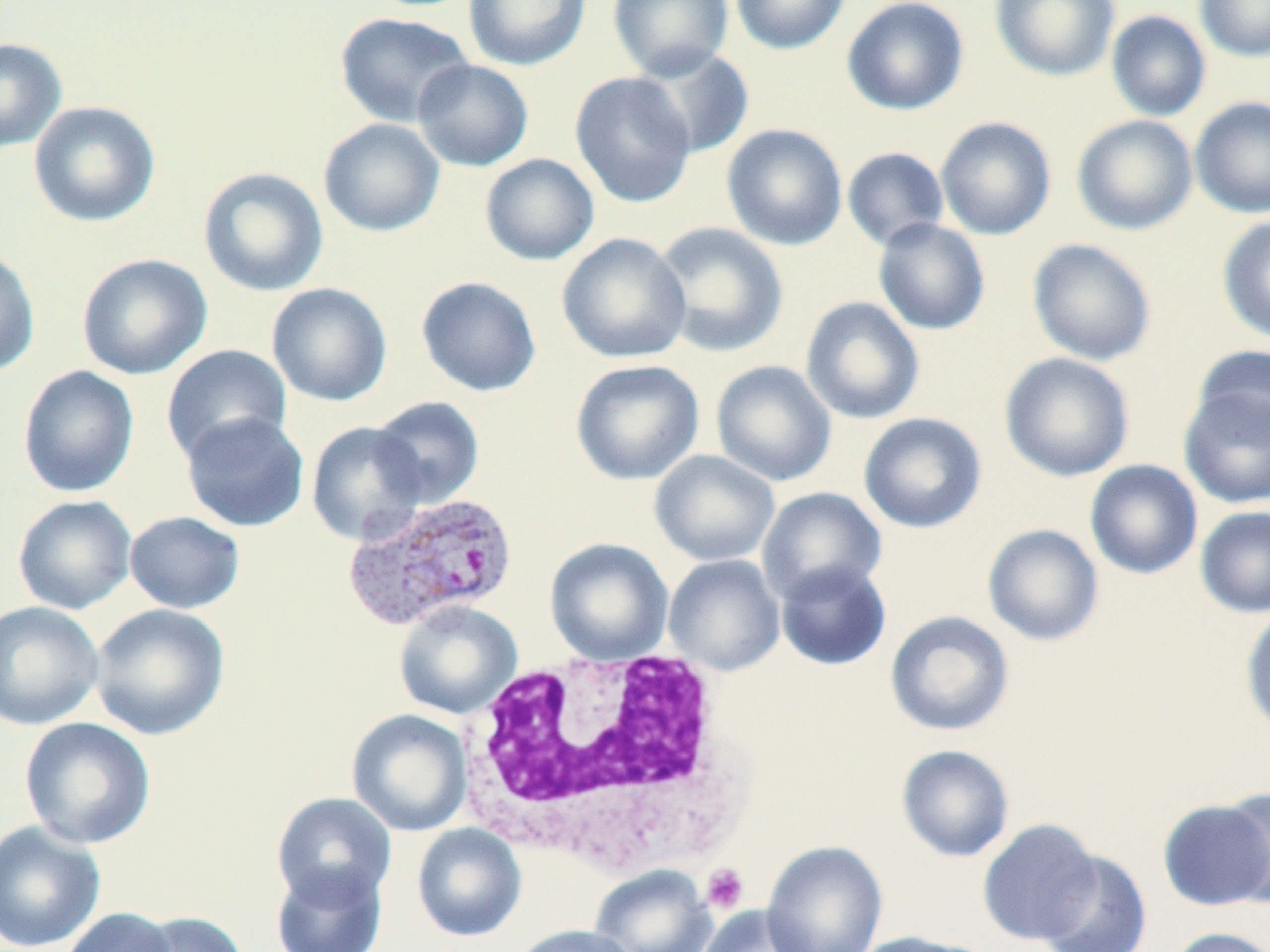

Summary:
  - Coordinate format: approximate bounding boxes as [x1, y1, x2, y2] in pixels
  - White blood cell locations: [455, 646, 748, 878]
  - Plasmodium vivax-infected red blood cell locations: [343, 491, 518, 631]
  - Platelet locations: [700, 863, 749, 913]
  - Uninfected red blood cell locations: [462, 0, 592, 71], [607, 0, 734, 80], [730, 0, 851, 55], [842, 0, 968, 116], [990, 0, 1120, 82], [1194, 0, 1270, 61], [1105, 10, 1211, 122], [334, 12, 475, 127], [0, 38, 67, 154], [630, 45, 755, 159], [413, 59, 534, 171], [569, 72, 697, 208], [1190, 96, 1270, 218], [28, 100, 161, 227], [1071, 114, 1198, 235], [935, 116, 1056, 240], [318, 117, 445, 238], [721, 123, 848, 251], [842, 147, 949, 251], [479, 153, 600, 266], [198, 167, 329, 297], [1217, 215, 1270, 344], [872, 218, 991, 335], [652, 221, 789, 358], [557, 232, 691, 364], [1026, 238, 1156, 366], [0, 245, 40, 377], [76, 253, 213, 380], [416, 276, 542, 397], [267, 283, 392, 406], [800, 296, 925, 425], [161, 344, 292, 464], [1191, 346, 1270, 447], [1000, 352, 1135, 482], [710, 359, 837, 487], [570, 360, 704, 485], [17, 365, 140, 498], [1178, 387, 1270, 509], [371, 395, 485, 508], [181, 412, 310, 532], [858, 412, 987, 534], [305, 420, 428, 546], [649, 450, 780, 567], [1084, 459, 1203, 580], [756, 486, 887, 604], [12, 494, 137, 614], [1194, 506, 1270, 618], [124, 510, 245, 614], [983, 523, 1104, 647], [544, 538, 674, 666], [663, 554, 786, 676], [774, 559, 892, 671], [0, 600, 104, 730], [393, 600, 523, 720], [89, 603, 230, 741], [1240, 607, 1270, 739], [885, 610, 1015, 736], [346, 709, 473, 836], [19, 716, 156, 849], [896, 744, 1015, 862], [1220, 787, 1270, 908], [271, 792, 397, 907], [1158, 797, 1270, 911], [977, 817, 1104, 946], [0, 820, 106, 952], [411, 823, 527, 942], [762, 841, 888, 952], [1037, 850, 1152, 952], [270, 860, 388, 952], [589, 864, 716, 952], [696, 905, 814, 952], [61, 907, 180, 952], [132, 910, 250, 952], [510, 924, 639, 952], [1166, 926, 1270, 952], [846, 931, 986, 952]
  - Slide-level diagnosis: Plasmodium vivax
  - Preparation: thin blood film
  - Stain: May-Grünwald-Giemsa
  - Field of view: one of a larger specimen
  - Image size: 1270×952 pixels
  - Modality: light microscopy
  - Magnification: 1000x